Assess this cell for malaria.
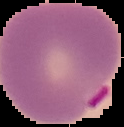

Parasitized.

Summary:
  - Image type: segmented cell region on a black background
  - Image size: 124×127 pixels
  - Preparation: thin blood smear